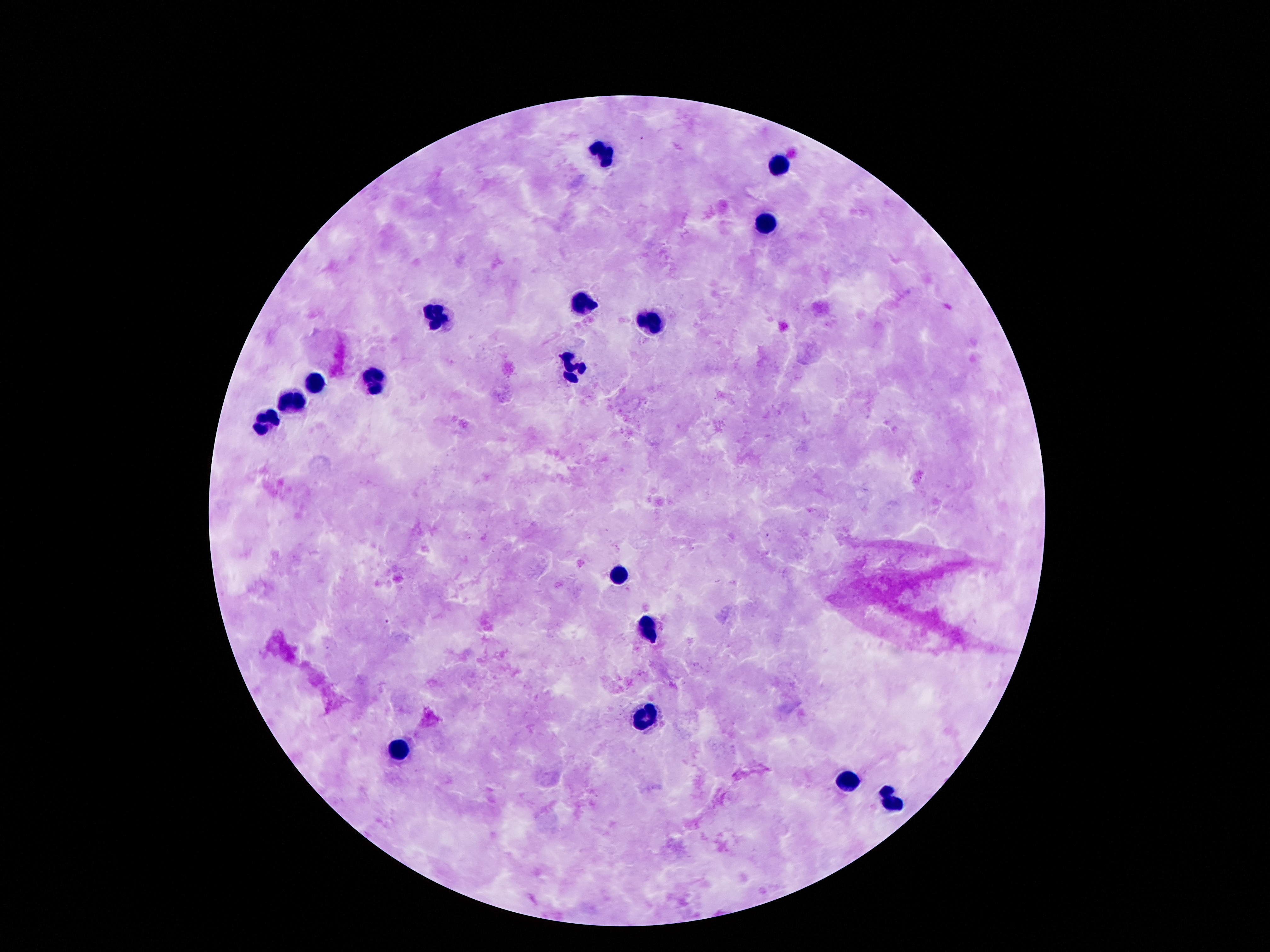

Approximate centers as {x, y} in pixels. Leukocyte locations: {604, 154}, {779, 165}, {764, 225}, {578, 305}, {432, 314}, {649, 319}, {574, 370}, {315, 381}, {376, 381}, {292, 403}, {264, 422}, {619, 577}, {647, 631}, {641, 717}, {402, 749}, {846, 781}, {891, 797}. Image is 1270×952 pixels. 100x magnification. Photographed through the microscope eyepiece with a smartphone camera. One field from this slide. Giemsa stain. Patient malaria status: not infected. Thick blood smear.